Locate every uninfected red blood cell.
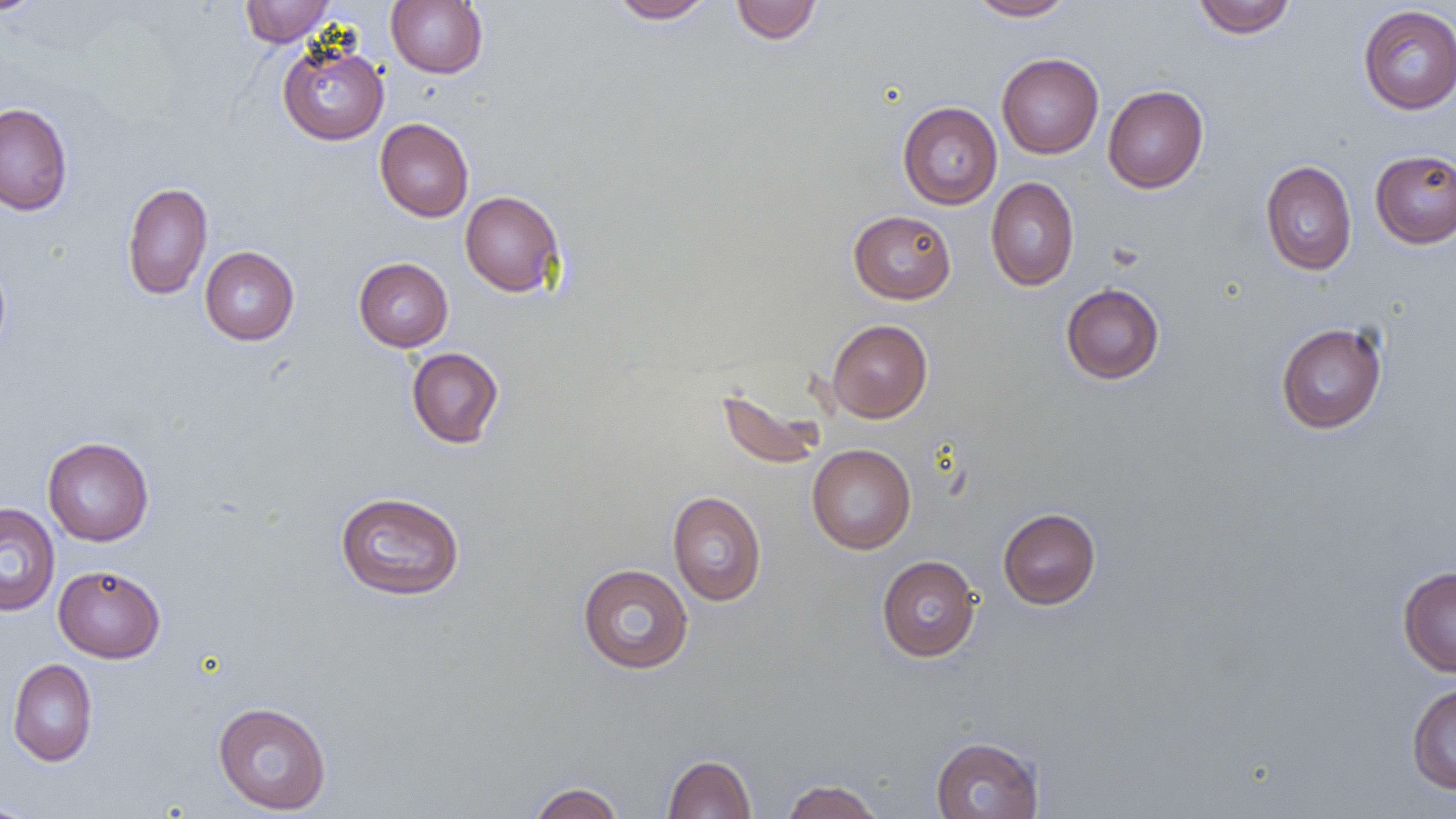
Approximate bounding boxes as [x1, y1, x2, y2] in pixels.
Uninfected red blood cells: [0, 0, 47, 16], [240, 0, 334, 47], [386, 0, 488, 78], [609, 0, 715, 23], [731, 0, 821, 44], [967, 0, 1077, 21], [1192, 0, 1297, 39], [1358, 5, 1456, 114], [277, 40, 389, 145], [996, 53, 1104, 159], [1103, 85, 1208, 193], [897, 101, 1002, 209], [0, 103, 73, 215], [375, 118, 474, 222], [1369, 149, 1456, 248], [1260, 160, 1357, 275], [986, 176, 1079, 291], [122, 182, 213, 300], [460, 191, 565, 296], [848, 210, 956, 304], [199, 246, 299, 345], [0, 253, 12, 359], [353, 257, 453, 352], [1061, 283, 1165, 385], [826, 319, 932, 423], [1275, 322, 1388, 434], [406, 347, 504, 449], [716, 386, 828, 471], [42, 436, 154, 546], [807, 444, 916, 554], [334, 490, 465, 600], [667, 490, 767, 606], [0, 503, 60, 616], [997, 507, 1101, 610], [876, 555, 981, 661], [53, 564, 165, 663], [577, 564, 694, 674], [1397, 566, 1456, 677], [8, 658, 97, 766], [1407, 683, 1456, 794], [213, 701, 332, 814], [930, 736, 1044, 819], [663, 754, 757, 818], [781, 779, 884, 819], [529, 782, 625, 819], [1, 798, 38, 818].

Slide-level diagnosis: negative for blood parasites. 1000x magnification. Thin blood film. Image is 1456×819 pixels. Optical microscopy. Single field of view.